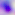

Summary:
  - Identification: Toxoplasma gondii
  - Magnification: 400x
  - Modality: micrograph